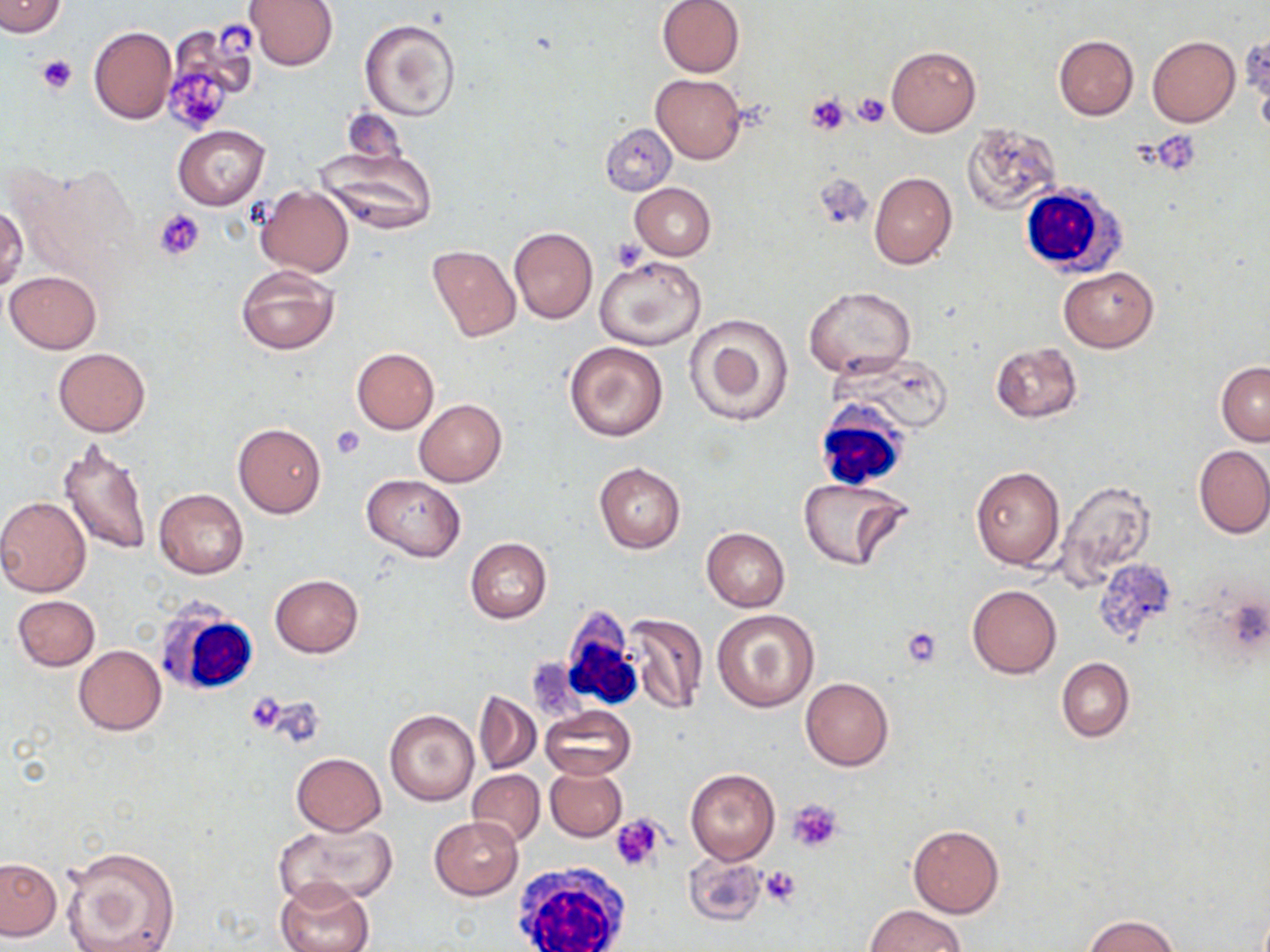
slide_level_diagnosis: negative for blood parasites
modality: light microscopy
stain: May-Grünwald-Giemsa
uninfected_red_blood_cell_locations: 'approximate bounding boxes as (x1, y1, x2, y2) in pixels: (244, 0, 339, 70), (657, 0, 745, 77), (0, 1, 66, 37), (360, 18, 460, 121), (164, 23, 261, 125), (88, 25, 176, 124), (1053, 35, 1139, 120), (1147, 35, 1240, 127), (886, 46, 980, 136), (651, 73, 746, 164), (343, 108, 406, 167), (598, 123, 675, 195), (962, 123, 1062, 213), (173, 125, 269, 210), (315, 145, 441, 235), (869, 171, 957, 270), (630, 182, 715, 260), (255, 186, 354, 276), (0, 206, 26, 291), (508, 227, 597, 323), (427, 245, 520, 341), (595, 256, 706, 352), (236, 265, 338, 355), (1058, 267, 1158, 352), (5, 270, 101, 353), (803, 285, 916, 378), (684, 312, 795, 426), (564, 341, 667, 441), (990, 343, 1082, 422), (53, 347, 150, 437), (351, 348, 439, 433), (1217, 362, 1270, 447), (414, 400, 507, 487), (232, 423, 327, 518), (57, 436, 153, 557), (1194, 444, 1270, 539), (594, 462, 685, 553), (971, 465, 1065, 570), (362, 475, 467, 560), (797, 476, 913, 573), (1055, 480, 1157, 589), (155, 488, 248, 579), (0, 495, 91, 596), (702, 528, 790, 611), (465, 537, 552, 623), (1091, 560, 1175, 644), (269, 574, 362, 657), (966, 585, 1061, 678), (12, 595, 100, 670), (712, 609, 819, 712), (622, 612, 708, 716), (73, 645, 166, 735), (1056, 658, 1134, 741), (800, 677, 893, 771), (474, 691, 541, 774), (541, 705, 636, 780), (386, 709, 479, 805), (290, 753, 385, 836), (544, 766, 626, 842), (467, 769, 544, 846), (686, 769, 779, 865), (429, 817, 523, 899), (275, 822, 397, 908), (908, 823, 1004, 916), (61, 846, 180, 952), (684, 853, 768, 927), (0, 858, 62, 941), (275, 878, 375, 952), (865, 904, 966, 951), (1083, 914, 1182, 952)'
field_of_view: single
preparation: thin blood film
image_size: 1270×952 pixels
white_blood_cell_locations: 'approximate bounding boxes as (x1, y1, x2, y2) in pixels: (1018, 182, 1124, 277), (813, 408, 908, 492), (155, 603, 260, 700), (556, 609, 643, 710), (511, 861, 634, 951)'
platelet_locations: 'approximate bounding boxes as (x1, y1, x2, y2) in pixels: (216, 22, 257, 60), (37, 55, 77, 94), (168, 74, 229, 132), (851, 91, 890, 126), (805, 94, 851, 136), (1150, 132, 1200, 175), (814, 175, 873, 230), (156, 208, 205, 259), (611, 237, 647, 272), (329, 425, 366, 459), (901, 626, 944, 667), (244, 691, 288, 736), (788, 799, 843, 853), (610, 814, 667, 872), (685, 856, 770, 927), (760, 865, 803, 909)'
magnification: 1000x